Comment on the morphology of the red blood cells.
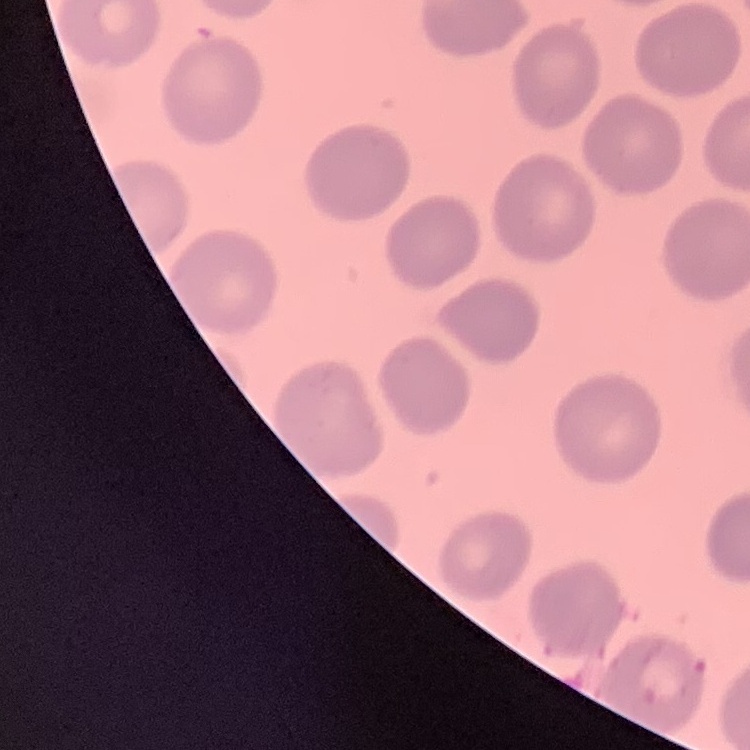
No rouleaux formation.

stain = Field's or Giemsa
image type = one tile cut from a larger photomicrograph
preparation = thin blood smear